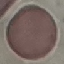
result = no malaria parasites detected
capture = smartphone through the microscope eyepiece
image type = automatically extracted cell patch, resized to 64 × 64 pixels
preparation = thin blood smear
stain = Giemsa